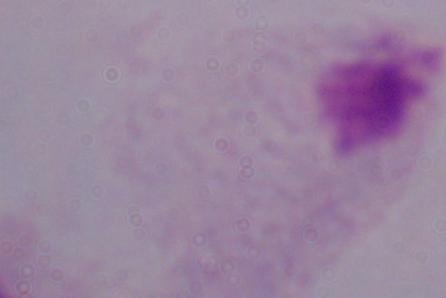

identification = trichomonad
magnification = 1000x
modality = micrograph